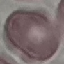
Malaria status: uninfected. Cell patch, automatically extracted from a larger field of view and resized to 64 × 64 pixels. Thin smear of blood. Giemsa-stained preparation. Acquired by smartphone through the microscope eyepiece.